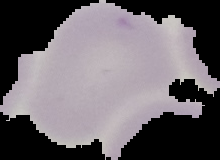

From a thin blood smear. Cell region segmented out of the field of view; the surrounding area is masked to black. Image is 220×160 pixels. Malaria status: uninfected.